Report the malaria status of this cell.
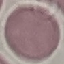
It is uninfected.

Giemsa stain. Acquired by smartphone through the microscope eyepiece. Thin blood film. Automatically extracted cell patch, resized to 64 × 64 pixels.